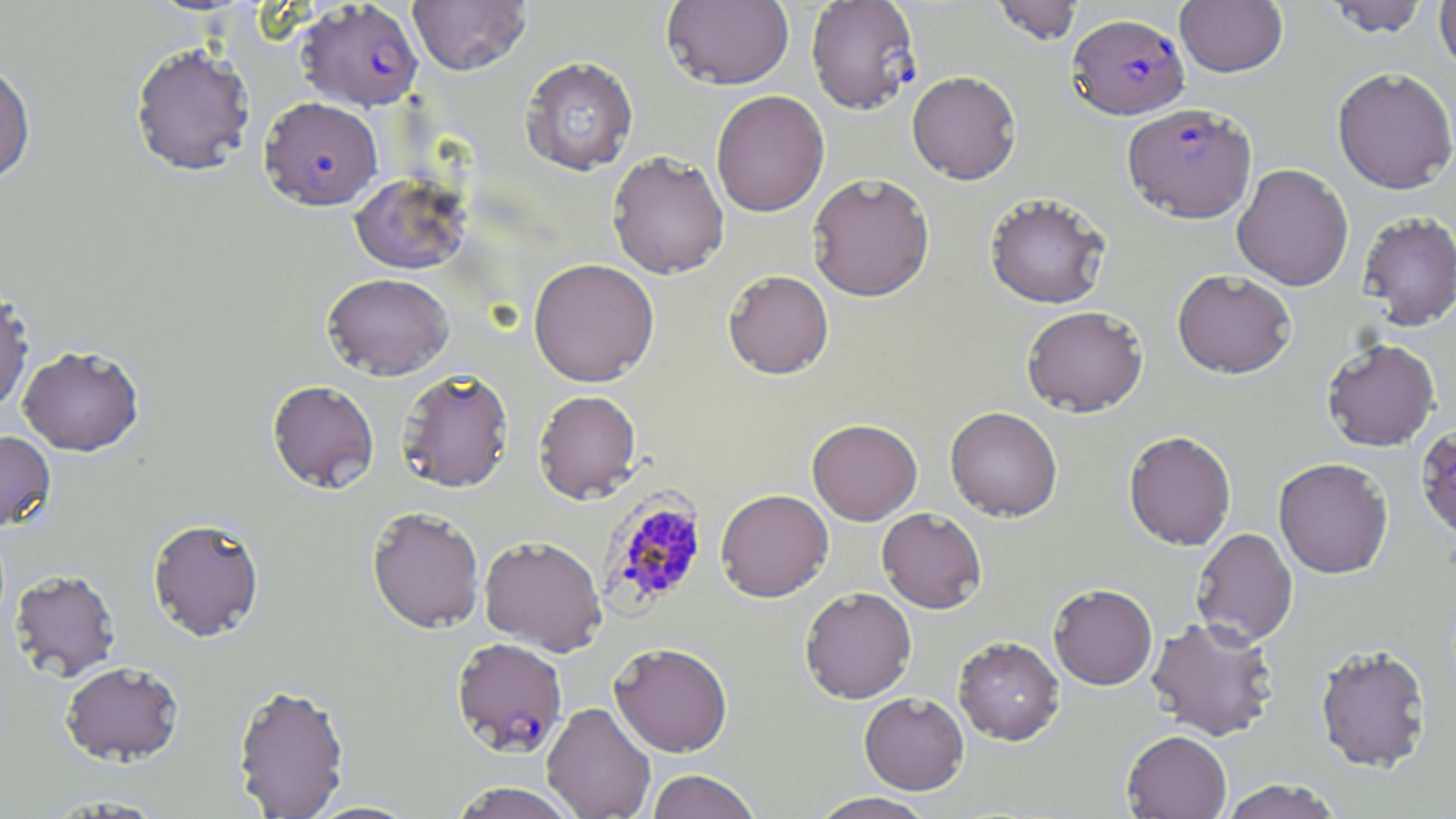

Summary:
  - Coordinate format: approximate bounding boxes as [x1, y1, x2, y2] in pixels
  - Uninfected red blood cell locations: [408, 0, 531, 75], [989, 0, 1083, 45], [1321, 0, 1431, 37], [662, 1, 794, 91], [1175, 1, 1287, 77], [1434, 1, 1456, 76], [130, 42, 256, 176], [519, 56, 639, 176], [0, 60, 36, 186], [1332, 66, 1456, 194], [906, 71, 1022, 184], [711, 90, 830, 217], [607, 151, 730, 278], [1232, 163, 1353, 291], [807, 172, 935, 301], [350, 173, 471, 274], [985, 192, 1111, 309], [1356, 210, 1456, 331], [528, 258, 659, 386], [1172, 269, 1296, 379], [723, 270, 834, 379], [323, 272, 454, 379], [0, 282, 34, 414], [1021, 305, 1148, 417], [1321, 338, 1440, 451], [18, 344, 144, 456], [397, 368, 514, 493], [267, 380, 380, 494], [533, 390, 642, 504], [945, 406, 1063, 521], [807, 418, 922, 525], [1415, 423, 1456, 543], [0, 429, 56, 532], [1123, 430, 1237, 550], [1273, 457, 1393, 578], [716, 489, 834, 602], [367, 506, 485, 633], [877, 507, 987, 613], [147, 517, 265, 641], [1191, 528, 1298, 646], [479, 535, 607, 655], [9, 568, 121, 682], [1048, 583, 1158, 690], [800, 587, 917, 704], [1146, 616, 1280, 742], [953, 636, 1065, 745], [609, 641, 733, 756], [1315, 643, 1433, 773], [60, 661, 184, 765], [232, 682, 350, 819], [859, 692, 969, 795], [542, 702, 655, 819], [1122, 730, 1231, 819], [646, 769, 762, 819], [1219, 779, 1345, 819], [449, 782, 579, 819], [808, 792, 938, 819], [37, 793, 171, 816], [304, 800, 423, 818]
  - Plasmodium falciparum-infected red blood cell locations: [806, 0, 922, 114], [297, 1, 423, 111], [1068, 13, 1190, 120], [260, 96, 383, 210], [1122, 103, 1257, 223], [599, 490, 709, 615], [451, 637, 567, 756]
  - Slide-level diagnosis: Plasmodium falciparum
  - Modality: light microscopy
  - Stain: May-Grünwald-Giemsa
  - Preparation: thin blood smear
  - Field of view: one of a larger specimen
  - Image size: 1456×819 pixels
  - Magnification: 1000x